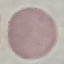

Summary:
  - Malaria status: uninfected
  - Stain: Giemsa
  - Image type: automatically extracted cell patch, resized to 64 × 64 pixels
  - Preparation: thin blood smear
  - Capture: smartphone camera at the microscope eyepiece